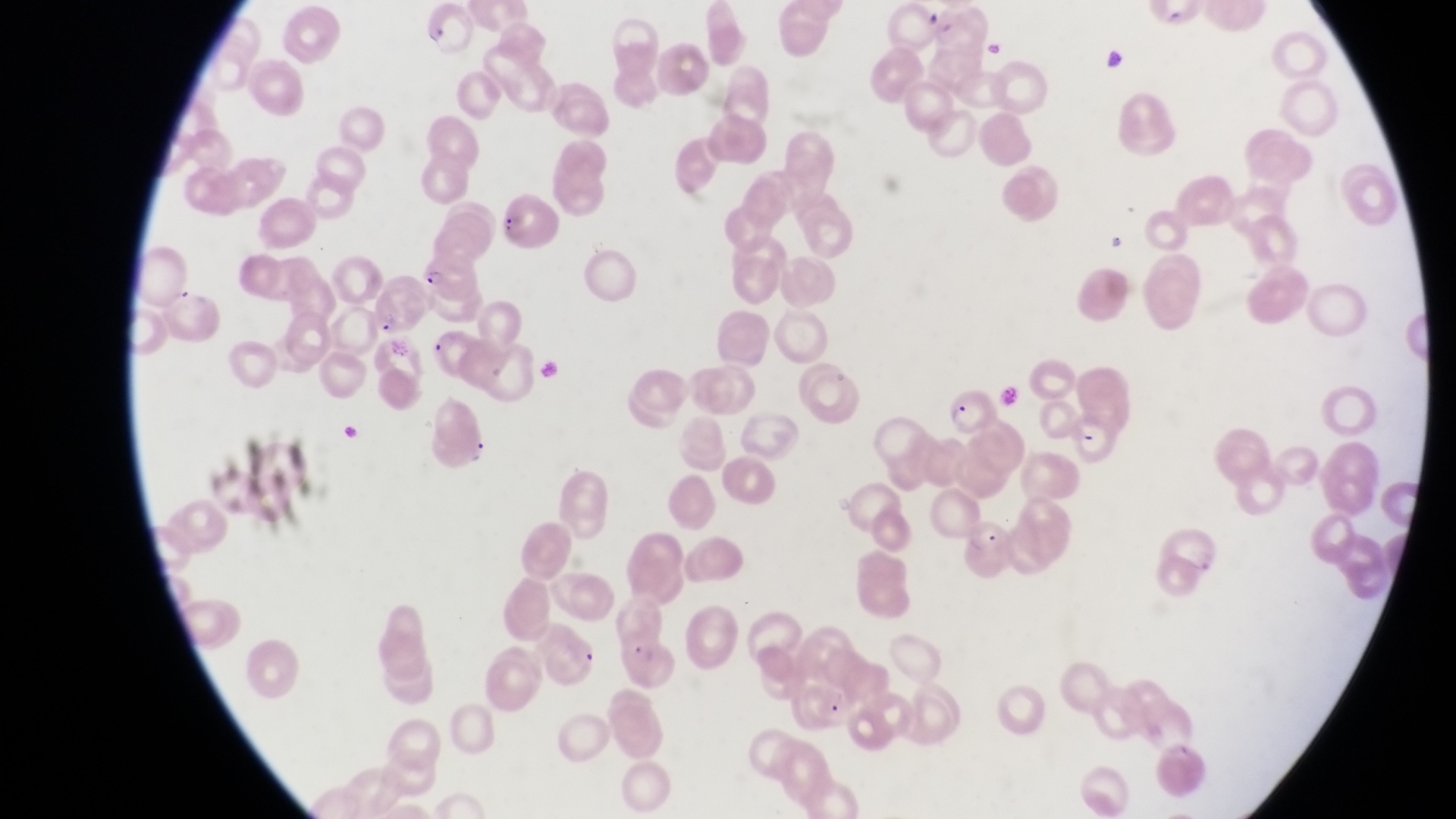

Approximate bounding boxes as [left, top, right, bottom] in pixels.
Summary:
  - Parasitised red blood cell locations: [426, 5, 482, 58], [497, 195, 563, 258], [417, 253, 480, 305], [375, 278, 427, 333], [423, 325, 484, 377], [944, 389, 993, 439], [1072, 413, 1125, 465], [952, 512, 1019, 576]
  - Artifact (platelet-like body, stain precipitate, or debris) locations: [1103, 47, 1137, 80], [1100, 227, 1132, 257]
  - Field of view: single
  - Capture: smartphone photograph through the eyepiece of an Olympus CX-23 microscope
  - Image size: 1456×819 pixels
  - Magnification: 1000x
  - Country: Uganda
  - Preparation: thin blood smear